Give the extent of all Plasmodium falciparum-infected red blood cells.
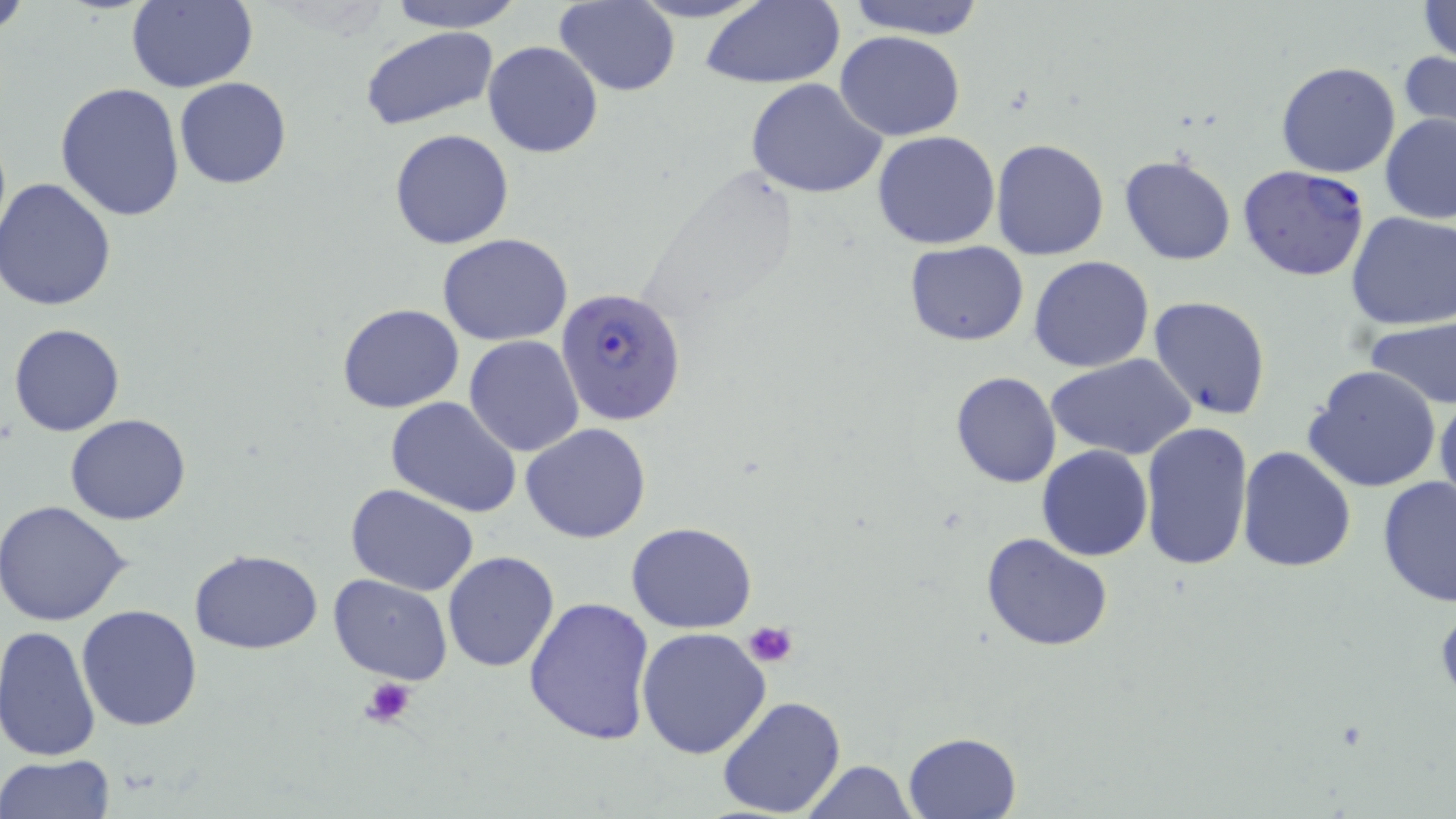
Approximate bounding boxes as [x1, y1, x2, y2] in pixels.
Plasmodium falciparum-infected red blood cells: [1237, 164, 1369, 281], [556, 284, 688, 426].

slide-level diagnosis = Plasmodium falciparum
platelet locations = approximate bounding boxes as [x1, y1, x2, y2] in pixels: [744, 619, 799, 667], [361, 676, 417, 729]
image size = 1456×819 pixels
magnification = 1000x
stain = May-Grünwald-Giemsa
modality = optical microscopy
uninfected red blood cell locations = approximate bounding boxes as [x1, y1, x2, y2] in pixels: [0, 0, 32, 40], [126, 0, 258, 94], [386, 0, 525, 30], [555, 0, 680, 96], [700, 0, 846, 89], [842, 0, 987, 39], [1417, 1, 1456, 63], [359, 26, 499, 130], [835, 29, 965, 141], [481, 40, 604, 159], [1401, 49, 1456, 136], [1276, 61, 1402, 179], [174, 77, 292, 190], [744, 77, 888, 199], [55, 80, 187, 221], [1379, 112, 1456, 223], [389, 130, 513, 249], [872, 130, 1001, 250], [991, 138, 1109, 260], [1120, 154, 1236, 266], [0, 179, 117, 312], [1344, 211, 1456, 331], [437, 234, 573, 346], [904, 241, 1029, 346], [1028, 257, 1154, 373], [1147, 296, 1272, 421], [337, 302, 466, 414], [1363, 314, 1456, 412], [8, 322, 126, 437], [464, 335, 584, 457], [1046, 354, 1196, 459], [1303, 366, 1444, 494], [949, 371, 1061, 489], [1435, 389, 1456, 521], [387, 397, 521, 517], [66, 414, 193, 525], [1139, 421, 1254, 572], [520, 422, 652, 544], [1237, 444, 1358, 573], [1036, 445, 1152, 562], [1377, 475, 1456, 608], [346, 484, 479, 597], [0, 500, 132, 626], [627, 522, 759, 633], [981, 532, 1114, 653], [189, 549, 325, 654], [443, 551, 560, 673], [328, 573, 454, 684], [524, 595, 657, 746], [76, 604, 203, 733], [0, 625, 102, 762], [637, 627, 772, 759], [718, 695, 848, 819], [903, 731, 1021, 817], [0, 753, 116, 819], [800, 760, 917, 818]
field of view = single
preparation = thin blood smear